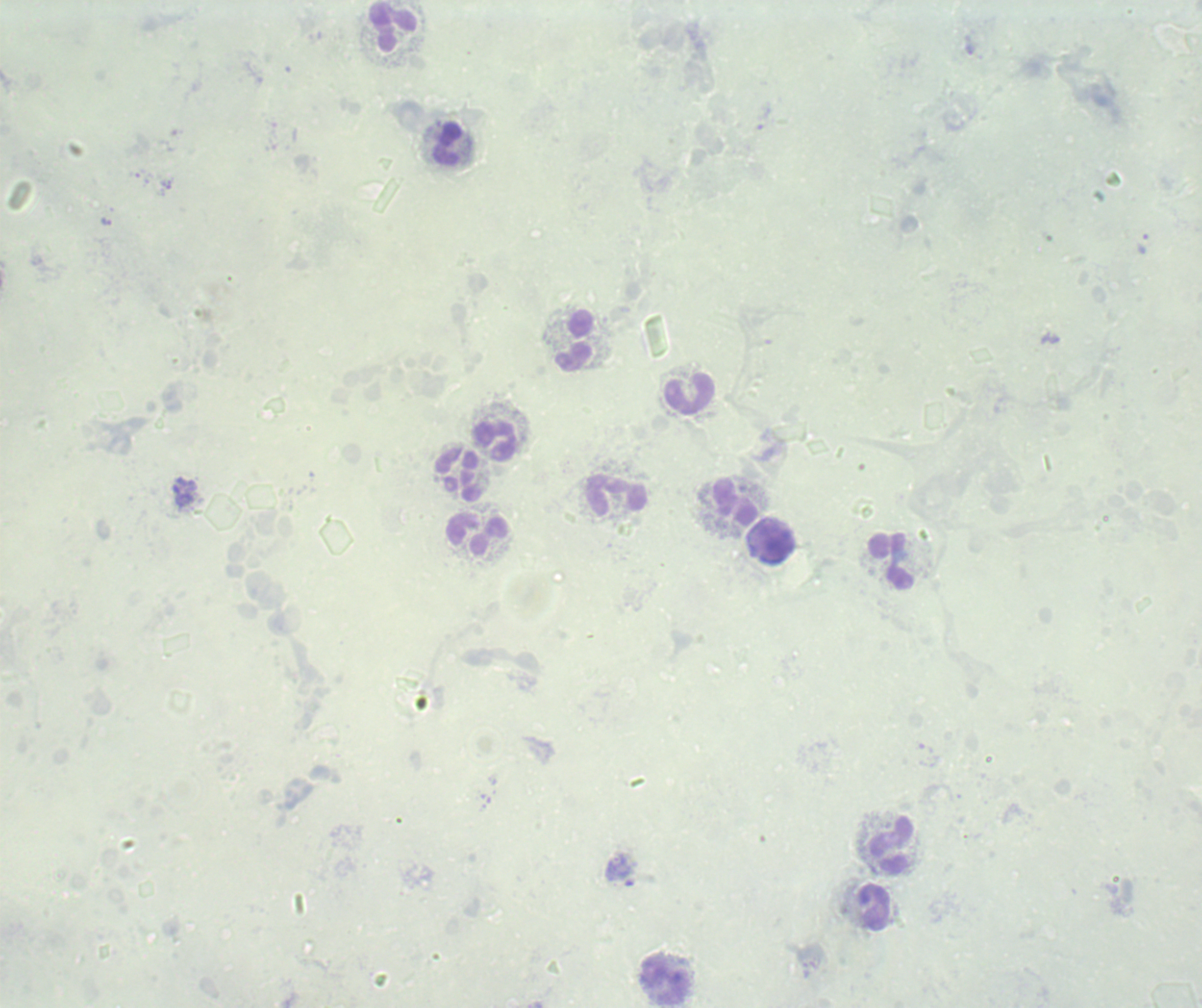

Approximate centers as (x, y) in pixels.
Summary:
  - Leukocyte locations: (394, 27), (448, 144), (574, 339), (689, 393), (496, 440), (460, 475), (617, 496), (736, 502), (477, 535), (772, 542), (892, 562), (892, 846), (874, 907), (666, 982)
  - Trophozoite locations: (1142, 243)
  - Result: malaria parasites detected
  - Image size: 1202×1008 pixels
  - Background quality: unsatisfactory
  - Stain: Romanowsky
  - Field of view: single
  - Context: previously used in a real diagnosis
  - Preparation: thick smear of blood
  - Magnification: 100x